State the blood parasite species.
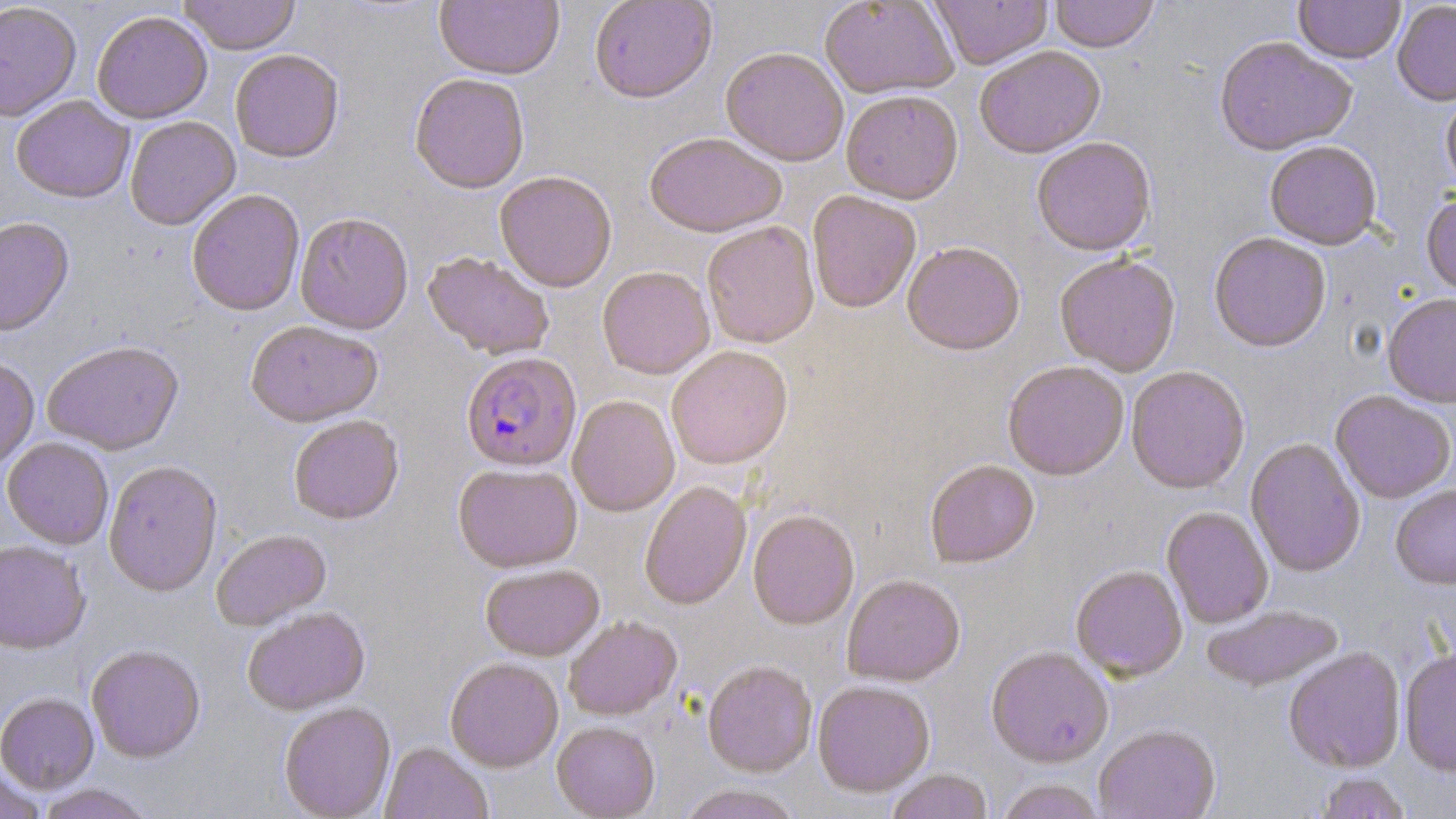
Plasmodium falciparum.

Summary:
  - Coordinate format: approximate bounding boxes as named x1/y1/x2/y2 corners in pixels
  - Plasmodium falciparum-infected red blood cell locations: (x1=461, y1=351, x2=582, y2=471)
  - Uninfected red blood cell locations: (x1=179, y1=0, x2=301, y2=55), (x1=589, y1=0, x2=717, y2=102), (x1=820, y1=0, x2=958, y2=98), (x1=930, y1=0, x2=1052, y2=69), (x1=1049, y1=0, x2=1160, y2=52), (x1=1294, y1=0, x2=1405, y2=64), (x1=0, y1=1, x2=81, y2=121), (x1=434, y1=1, x2=564, y2=80), (x1=1392, y1=1, x2=1456, y2=107), (x1=92, y1=10, x2=213, y2=123), (x1=1213, y1=35, x2=1356, y2=156), (x1=974, y1=45, x2=1105, y2=159), (x1=721, y1=47, x2=848, y2=166), (x1=230, y1=49, x2=344, y2=162), (x1=409, y1=72, x2=529, y2=193), (x1=841, y1=89, x2=963, y2=204), (x1=1441, y1=91, x2=1456, y2=197), (x1=11, y1=95, x2=134, y2=203), (x1=124, y1=116, x2=241, y2=229), (x1=644, y1=132, x2=787, y2=237), (x1=1031, y1=136, x2=1156, y2=255), (x1=1265, y1=141, x2=1382, y2=250), (x1=494, y1=170, x2=617, y2=292), (x1=186, y1=188, x2=305, y2=316), (x1=806, y1=190, x2=922, y2=313), (x1=1422, y1=192, x2=1456, y2=301), (x1=295, y1=212, x2=414, y2=334), (x1=0, y1=216, x2=74, y2=337), (x1=701, y1=221, x2=819, y2=348), (x1=1209, y1=232, x2=1331, y2=352), (x1=902, y1=240, x2=1025, y2=355), (x1=423, y1=251, x2=555, y2=359), (x1=1055, y1=253, x2=1181, y2=376), (x1=597, y1=266, x2=715, y2=378), (x1=1382, y1=292, x2=1456, y2=408), (x1=245, y1=320, x2=382, y2=427), (x1=42, y1=339, x2=184, y2=455), (x1=666, y1=345, x2=792, y2=469), (x1=0, y1=355, x2=39, y2=472), (x1=1002, y1=360, x2=1129, y2=480), (x1=1126, y1=366, x2=1250, y2=494), (x1=1331, y1=391, x2=1455, y2=504), (x1=567, y1=395, x2=680, y2=516), (x1=288, y1=414, x2=404, y2=524), (x1=1, y1=437, x2=114, y2=549), (x1=1245, y1=438, x2=1366, y2=577), (x1=103, y1=459, x2=222, y2=596), (x1=925, y1=459, x2=1040, y2=567), (x1=453, y1=462, x2=582, y2=572), (x1=639, y1=480, x2=751, y2=609), (x1=1390, y1=485, x2=1456, y2=589), (x1=1162, y1=506, x2=1274, y2=627), (x1=747, y1=508, x2=859, y2=629), (x1=212, y1=529, x2=331, y2=630), (x1=0, y1=539, x2=91, y2=654), (x1=481, y1=564, x2=604, y2=660), (x1=1071, y1=564, x2=1187, y2=681), (x1=842, y1=574, x2=965, y2=686), (x1=1201, y1=605, x2=1344, y2=691), (x1=242, y1=606, x2=370, y2=715), (x1=563, y1=615, x2=682, y2=720), (x1=86, y1=644, x2=205, y2=763), (x1=986, y1=646, x2=1114, y2=766), (x1=1283, y1=647, x2=1406, y2=773), (x1=1400, y1=647, x2=1456, y2=776), (x1=445, y1=657, x2=563, y2=772), (x1=702, y1=659, x2=817, y2=777), (x1=812, y1=679, x2=935, y2=796), (x1=0, y1=692, x2=99, y2=793), (x1=279, y1=701, x2=396, y2=818), (x1=552, y1=721, x2=660, y2=818), (x1=1094, y1=724, x2=1221, y2=819), (x1=381, y1=742, x2=492, y2=819), (x1=0, y1=768, x2=47, y2=818), (x1=886, y1=769, x2=992, y2=819), (x1=1313, y1=772, x2=1412, y2=819), (x1=995, y1=778, x2=1106, y2=819), (x1=36, y1=784, x2=154, y2=818), (x1=678, y1=784, x2=802, y2=819)
  - Field of view: single
  - Image size: 1456×819 pixels
  - Modality: light microscopy
  - Magnification: 1000x
  - Preparation: thin blood smear
  - Stain: May-Grünwald-Giemsa